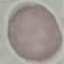
Summary:
  - Malaria status: uninfected
  - Preparation: thin smear
  - Capture: smartphone camera at the microscope eyepiece
  - Stain: Giemsa
  - Image type: cell patch, automatically extracted from a larger field of view and resized to 64 × 64 pixels